Classify this cell by malaria status.
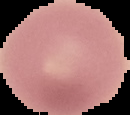
Uninfected.

Image is 130×115 pixels. The area outside the segmented cell region is set to black. From a thin blood smear.